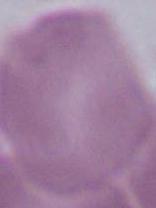
Summary:
  - Modality: photomicrograph
  - Magnification: 1000x
  - Identification: red blood cell